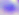

Summary:
  - Magnification: 400x
  - Modality: photomicrograph
  - Identification: Toxoplasma gondii